Name the parasite shown.
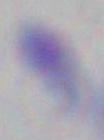
Toxoplasma gondii.

magnification = 1000x
modality = micrograph